Look for Plasmodium parasites.
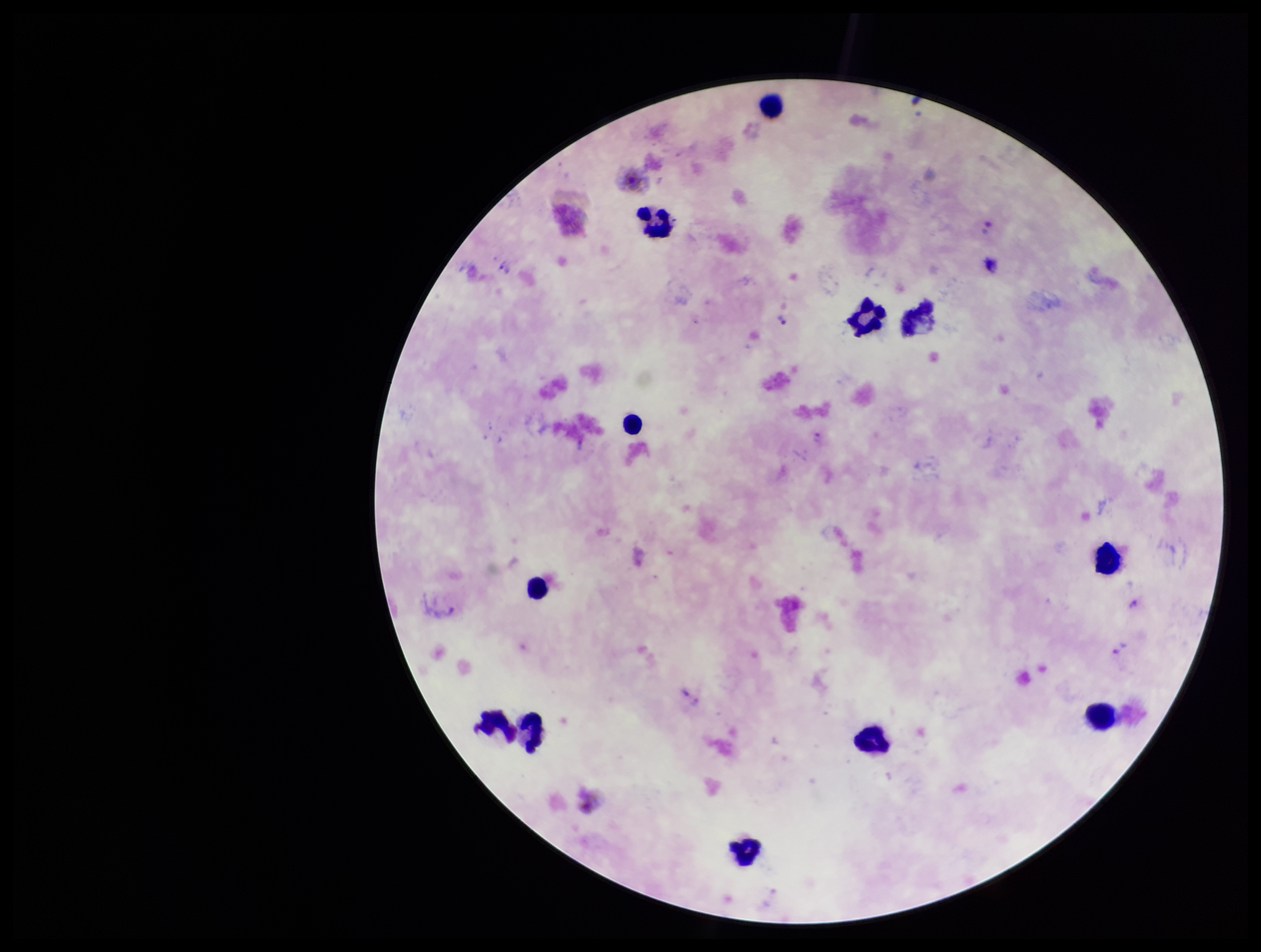
Seen.

Species reported for this patient: Plasmodium vivax. Parasite count: 1. Stained with Giemsa. Image is 1261×952 pixels. Preparation: thick blood smear. Leukocyte count: 12. Smartphone photograph taken through the eyepiece of a microscope. Patient malaria status: infected. Single field of view.